State which parasite is depicted.
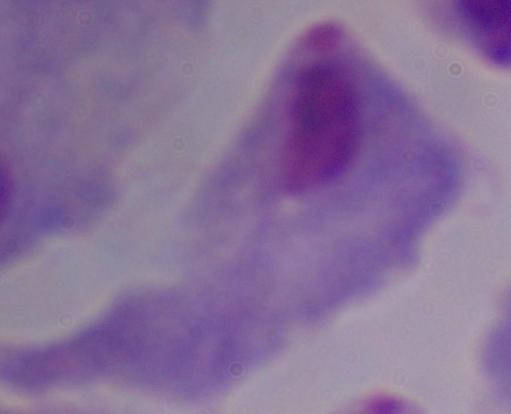

This is a trichomonad.

1000x magnification. Photomicrograph.